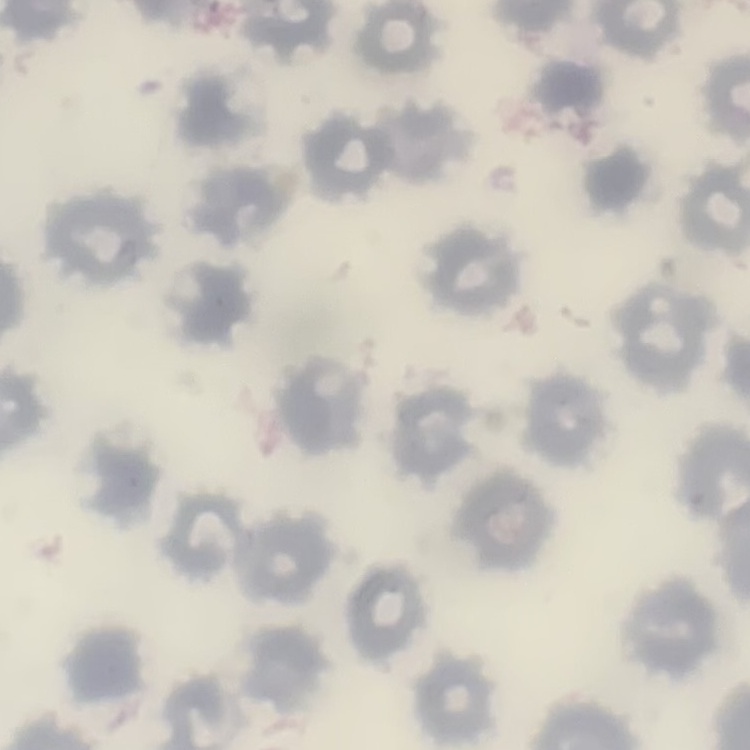
{
  "red_blood_cell_morphology": "no rouleaux formation",
  "preparation": "thin peripheral smear",
  "stain": "Field's or Giemsa",
  "image_type": "square crop of a larger photomicrograph"
}